Classify this cell by malaria status.
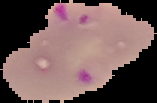

Parasitized.

image_type: cell region segmented out of the field of view; surrounding area masked to black
preparation: thin blood smear
image_size: 157×103 pixels